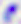
modality = photomicrograph
magnification = 400x
identification = Toxoplasma gondii